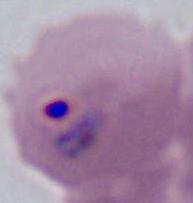
Summary:
  - Magnification: 400x or 1000x
  - Identification: Plasmodium
  - Modality: micrograph